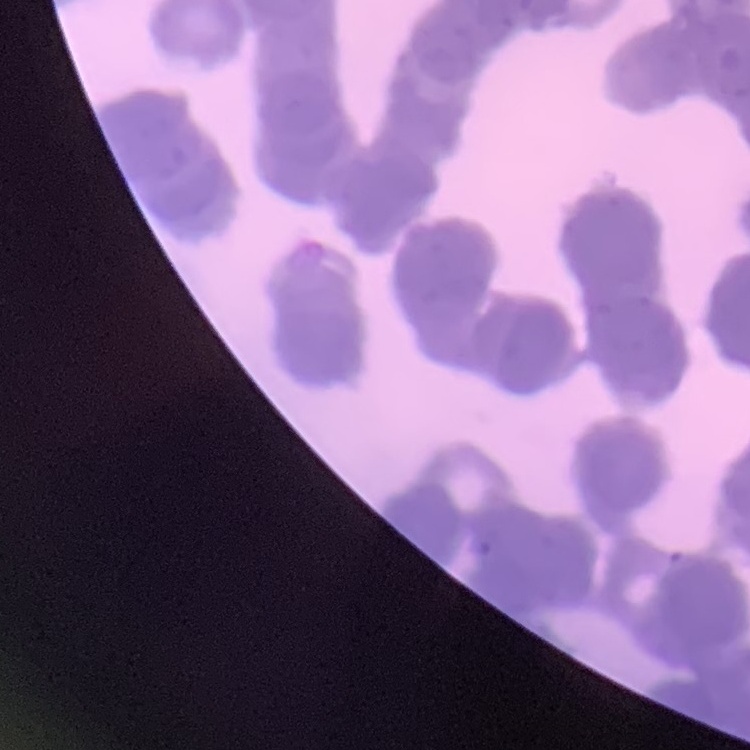 The erythrocytes exhibit rouleaux formation. Stained with either Field's or Giemsa. Thin blood smear. Square crop of a larger photomicrograph.